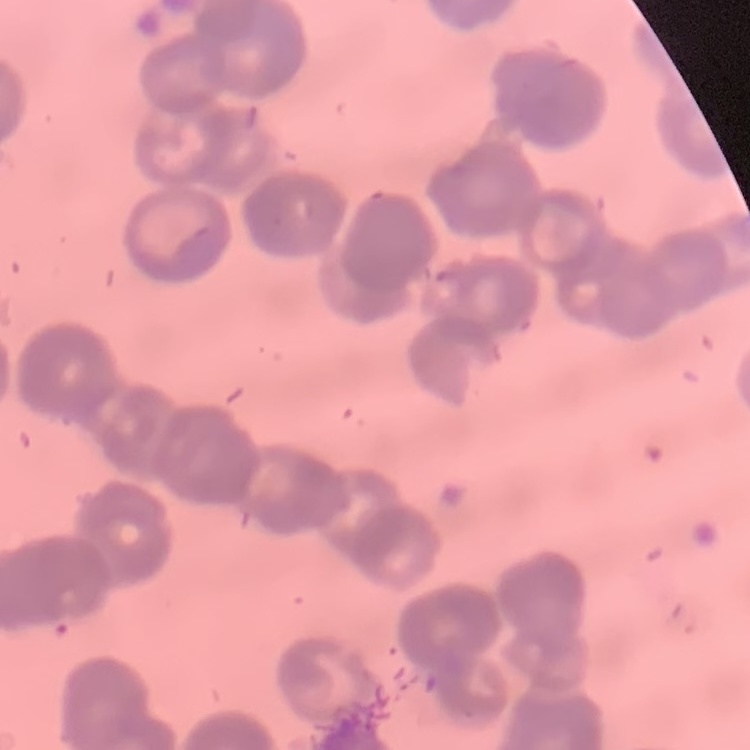

The erythrocytes exhibit rouleaux formation. Stained with either Field's or Giemsa. Thin blood smear. Square crop of a larger photomicrograph.